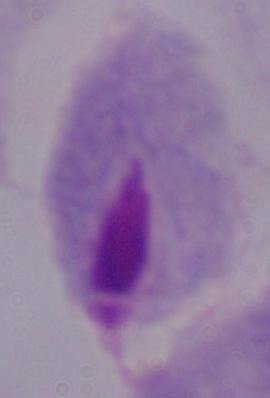

Captured at 1000x magnification. A trichomonad is shown. Photomicrograph.